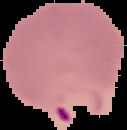
Image is 127×130 pixels. Malaria status: parasitized. Cell region segmented out of the field of view; the surrounding area is masked to black. From a thin blood film.